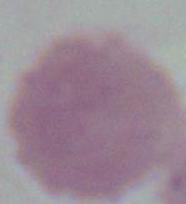 Captured at 1000x magnification. Photomicrograph. A red blood cell is seen.